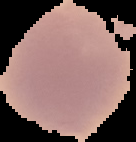

From a thin blood film. Image is 136×142 pixels. Cell region segmented out of the field of view; the surrounding area is masked to black. Result: no malaria parasites seen.